Classify this cell by malaria status.
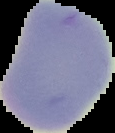

Uninfected.

The area outside the segmented cell region is set to black. Image is 115×133 pixels. From a thin blood smear.